Locate every leukocyte (white blood cell).
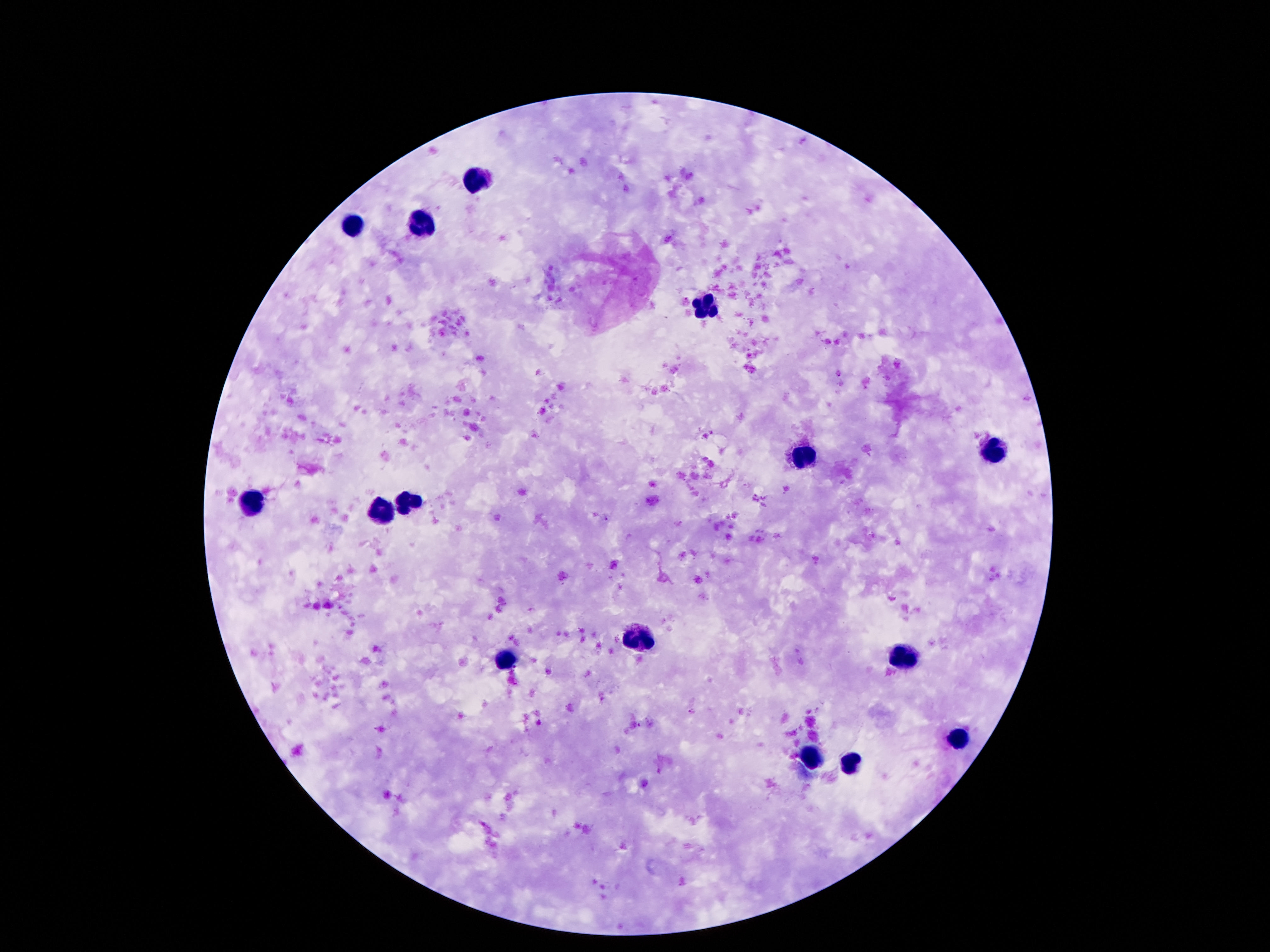

Approximate centers as [x, y] in pixels.
Leukocytes: [474, 176], [353, 223], [416, 224], [703, 310], [987, 450], [802, 459], [409, 501], [250, 502], [384, 510], [638, 641], [907, 656], [506, 662], [957, 737], [815, 757], [852, 765].

Photographed through the microscope eyepiece with a smartphone camera. Giemsa stain. Patient malaria status: not infected. Image is 1270×952 pixels. 100x magnification. Single field of view. Thick peripheral-blood smear.